Name the parasite shown.
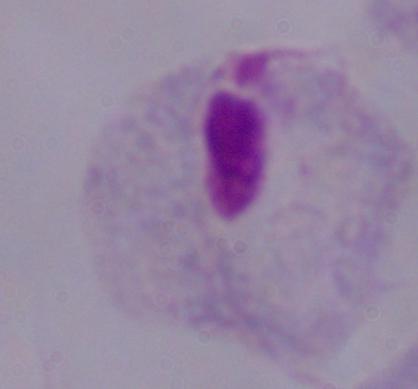

A trichomonad.

Summary:
  - Modality: micrograph
  - Magnification: 1000x